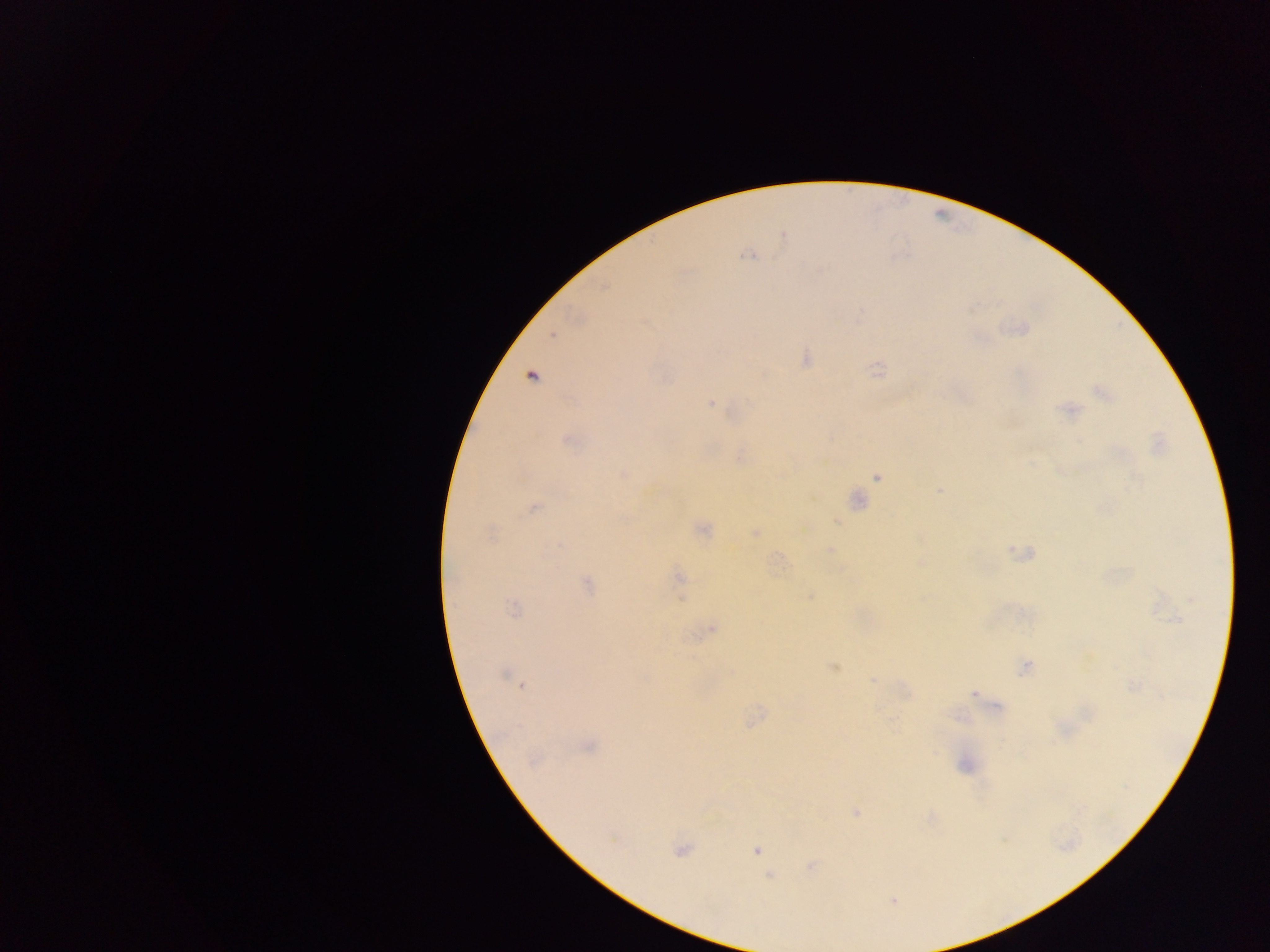

capture = mobile-phone photograph through a microscope
field of view = single
image size = 1270×952 pixels
malaria parasite locations = approximate centers as {x, y} in pixels: {747, 255}, {553, 334}, {709, 403}, {523, 478}, {879, 479}, {533, 507}, {490, 532}, {676, 574}, {711, 627}, {521, 686}, {976, 695}, {756, 851}, {894, 902}
country = Ghana
preparation = thick blood smear